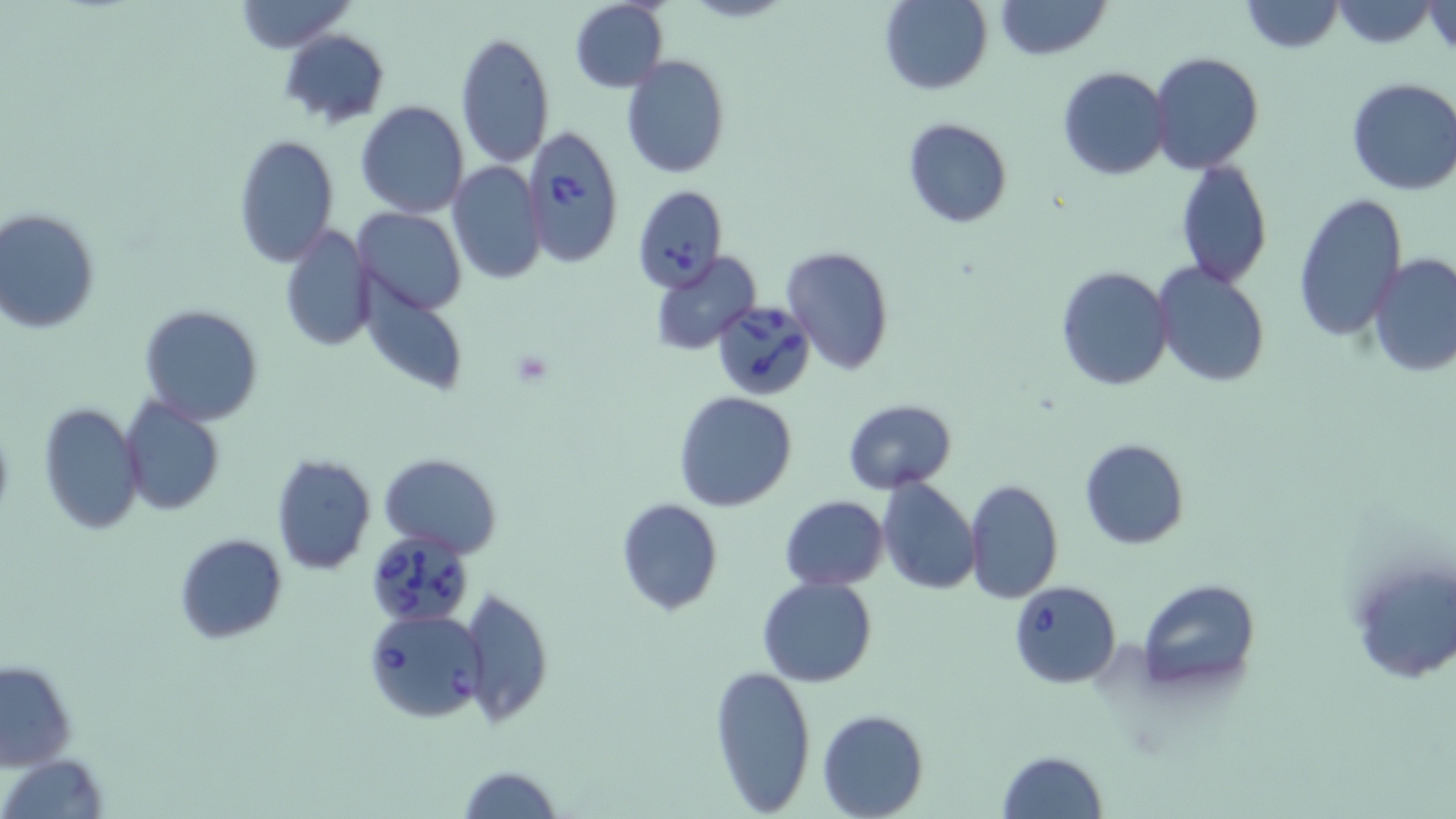
Approximate bounding boxes as (x1, y1, x2, y2) in pixels. Uninfected red blood cell locations: (233, 0, 354, 52), (996, 0, 1111, 60), (1237, 0, 1345, 52), (880, 1, 994, 95), (1329, 1, 1440, 48), (568, 2, 669, 91), (1425, 3, 1455, 55), (280, 29, 390, 129), (453, 32, 556, 169), (1149, 50, 1264, 174), (621, 56, 731, 178), (1057, 66, 1172, 181), (1345, 77, 1456, 196), (355, 101, 470, 219), (903, 118, 1012, 229), (232, 136, 340, 266), (1174, 159, 1273, 286), (447, 162, 547, 284), (1292, 191, 1406, 341), (0, 207, 101, 334), (354, 208, 465, 313), (1313, 215, 1452, 368), (279, 224, 375, 351), (781, 245, 894, 376), (652, 252, 760, 357), (1367, 252, 1456, 378), (1152, 262, 1270, 386), (1055, 265, 1175, 392), (139, 304, 266, 426), (675, 392, 798, 512), (119, 396, 226, 516), (843, 398, 958, 494), (38, 402, 146, 537), (1079, 438, 1189, 550), (270, 452, 376, 576), (380, 453, 501, 558), (876, 477, 981, 596), (964, 479, 1062, 604), (778, 495, 888, 591), (615, 498, 723, 616), (174, 533, 287, 642), (1347, 552, 1455, 687), (757, 575, 878, 687), (1138, 579, 1258, 691), (458, 586, 554, 728), (1, 659, 77, 771), (709, 663, 817, 815), (818, 710, 927, 818), (996, 750, 1107, 819), (2, 753, 110, 819), (458, 764, 562, 819). Platelet locations: (507, 349, 553, 387). Babesia divergens-infected red blood cell locations: (519, 126, 624, 269), (632, 184, 729, 294), (712, 298, 816, 401), (369, 531, 482, 624), (1008, 580, 1121, 687), (364, 609, 486, 724). Slide-level diagnosis: Babesia divergens. Captured at 1000x magnification. Light microscopy. May-Grünwald-Giemsa stain. Thin blood film. One field of a larger specimen. Image is 1456×819 pixels.